State which parasite is depicted.
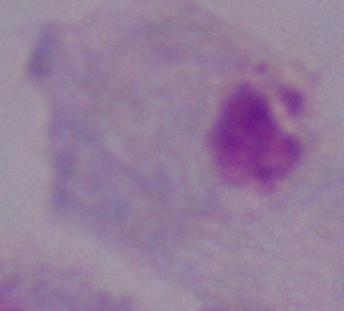
A trichomonad.

modality = photomicrograph
magnification = 1000x